Identify the parasite.
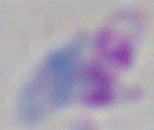
This is Toxoplasma gondii.

Photomicrograph. Captured at 1000x magnification.